Classify this cell by malaria status.
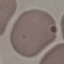
It is uninfected.

{
  "capture": "smartphone camera at the microscope eyepiece",
  "image_type": "automatically extracted cell patch, resized to 64 × 64 pixels",
  "preparation": "thin blood smear",
  "stain": "Giemsa"
}